State which cell type is depicted.
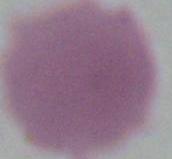

This is an erythrocyte.

Captured at 1000x magnification. Photomicrograph.